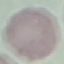
Summary:
  - Malaria status: uninfected
  - Preparation: thin blood film
  - Stain: Giemsa
  - Image type: cell patch, automatically extracted from a larger field of view and resized to 64 × 64 pixels
  - Capture: smartphone camera at the microscope eyepiece